Name the parasite shown.
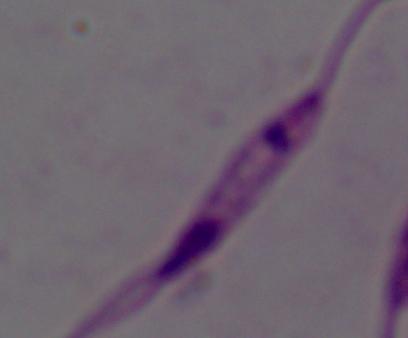
Leishmania.

Captured at 1000x magnification. Photomicrograph.